Identify the preparation type.
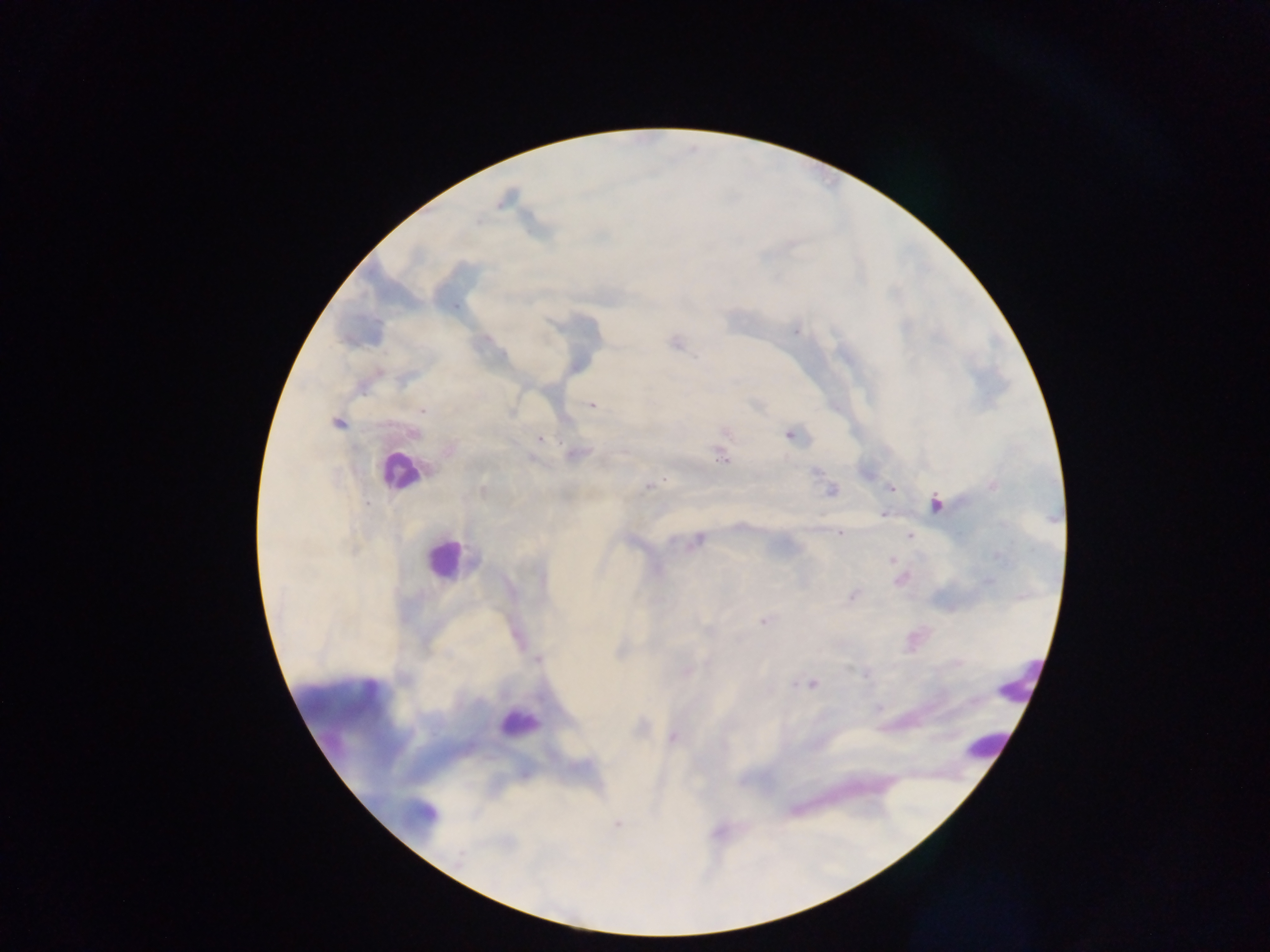

This is a thick smear.

Approximate centers as {x, y} in pixels.
Summary:
  - Plasmodium parasite locations: {796, 331}, {592, 405}, {422, 412}, {337, 422}, {414, 434}, {788, 435}, {541, 438}, {576, 454}, {722, 459}, {648, 485}, {890, 488}, {830, 491}, {935, 504}, {883, 513}, {840, 533}, {909, 536}, {699, 539}, {891, 560}, {852, 596}, {763, 621}, {709, 630}, {538, 659}, {686, 672}, {866, 674}, {795, 683}, {812, 684}, {672, 737}, {616, 825}, {458, 857}
  - Leukocyte locations: {398, 471}, {445, 559}, {1022, 682}, {517, 726}, {985, 750}
  - Country: Ghana
  - Image size: 1270×952 pixels
  - Capture: mobile-phone photograph through a microscope
  - Field of view: single